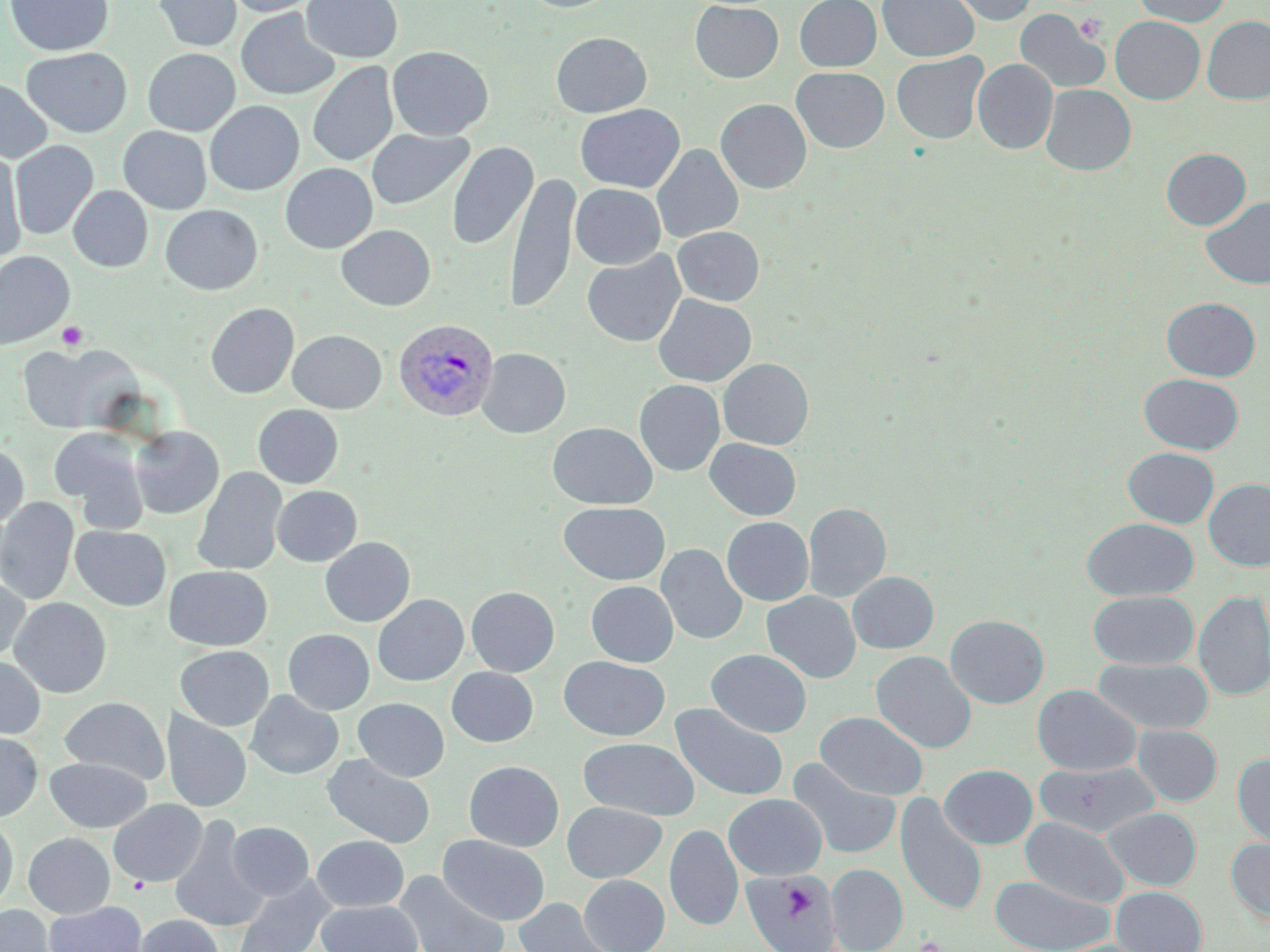

slide-level diagnosis = Plasmodium vivax
magnification = 1000x
Plasmodium vivax-infected red blood cell locations = approximate bounding boxes as (x1,y1)-(x2,y2) corner pairs in pixels: (393,318)-(499,422)
platelet locations = approximate bounding boxes as (x1,y1)-(x2,y2) corner pairs in pixels: (1075,13)-(1107,43), (56,321)-(89,351), (128,875)-(150,893), (916,935)-(943,952)
field of view = single
image size = 1270×952 pixels
stain = May-Grünwald-Giemsa
modality = optical microscopy
preparation = thin blood smear
uninfected red blood cell locations = approximate bounding boxes as (x1,y1)-(x2,y2) corner pairs in pixels: (4,0)-(114,57), (152,0)-(242,52), (223,0)-(323,17), (301,0)-(403,63), (518,0)-(619,13), (794,0)-(882,72), (877,0)-(979,62), (942,0)-(1039,26), (1132,0)-(1231,27), (689,1)-(784,83), (236,7)-(341,100), (1014,8)-(1109,95), (1110,15)-(1205,104), (1202,16)-(1270,105), (550,32)-(652,118), (387,46)-(494,140), (21,47)-(132,138), (142,48)-(240,136), (891,52)-(989,144), (972,58)-(1058,154), (307,61)-(399,167), (791,67)-(890,153), (0,79)-(53,163), (1041,84)-(1136,176), (715,99)-(812,194), (205,101)-(304,195), (575,103)-(685,193), (118,126)-(212,214), (367,129)-(474,210), (10,140)-(98,240), (447,142)-(538,251), (652,145)-(744,243), (1161,148)-(1251,230), (0,151)-(27,265), (280,163)-(378,254), (505,172)-(579,313), (570,184)-(666,269), (68,185)-(152,272), (1200,195)-(1270,290), (161,204)-(263,295), (336,224)-(436,311), (672,226)-(765,306), (0,251)-(74,349), (581,251)-(686,347), (652,294)-(756,387), (1161,297)-(1260,380), (205,302)-(299,398), (287,329)-(386,414), (18,343)-(137,434), (476,348)-(571,438), (718,358)-(814,449), (1139,373)-(1243,454), (634,379)-(725,476), (252,404)-(344,489), (547,422)-(658,509), (129,425)-(224,519), (49,427)-(149,527), (704,439)-(802,520), (0,442)-(29,530), (1122,447)-(1219,528), (193,467)-(287,576), (1204,478)-(1270,572), (272,485)-(362,566), (0,497)-(78,605), (558,502)-(671,585), (803,502)-(892,602), (721,517)-(813,606), (1081,518)-(1198,601), (71,525)-(171,611), (320,536)-(416,627), (656,543)-(748,645), (164,565)-(273,651), (847,571)-(939,654), (0,574)-(30,665), (585,580)-(678,667), (466,586)-(560,676), (1194,590)-(1270,702), (761,591)-(861,683), (1088,591)-(1198,670), (373,593)-(468,686), (9,597)-(112,698), (945,614)-(1049,709), (283,629)-(374,714), (175,645)-(274,731), (706,649)-(812,738), (870,650)-(977,753), (0,656)-(46,740), (559,656)-(670,741), (1093,657)-(1213,734), (446,667)-(538,747), (1032,684)-(1141,775), (245,690)-(344,780), (59,696)-(169,784), (353,697)-(449,782), (670,703)-(789,802), (161,710)-(252,813), (815,711)-(929,801), (1133,724)-(1222,805), (0,731)-(43,822), (578,738)-(699,820), (321,753)-(435,849), (1233,753)-(1270,850), (45,757)-(152,833), (788,758)-(901,860), (463,760)-(564,851), (1034,761)-(1160,838), (939,764)-(1037,849), (723,793)-(827,880), (895,793)-(988,916), (108,799)-(207,887), (562,802)-(667,883), (1102,806)-(1201,890), (169,815)-(267,933), (1020,816)-(1128,907), (0,818)-(18,910), (226,821)-(314,901), (664,824)-(744,931), (22,832)-(115,918), (438,834)-(550,925), (311,835)-(409,912), (1225,837)-(1270,926), (827,864)-(908,952), (742,870)-(841,952), (393,871)-(510,952), (579,874)-(670,952), (989,874)-(1114,952), (231,875)-(337,952), (1111,886)-(1207,952), (513,897)-(615,951), (316,900)-(423,952), (44,901)-(147,952), (0,905)-(57,952), (135,914)-(225,952)